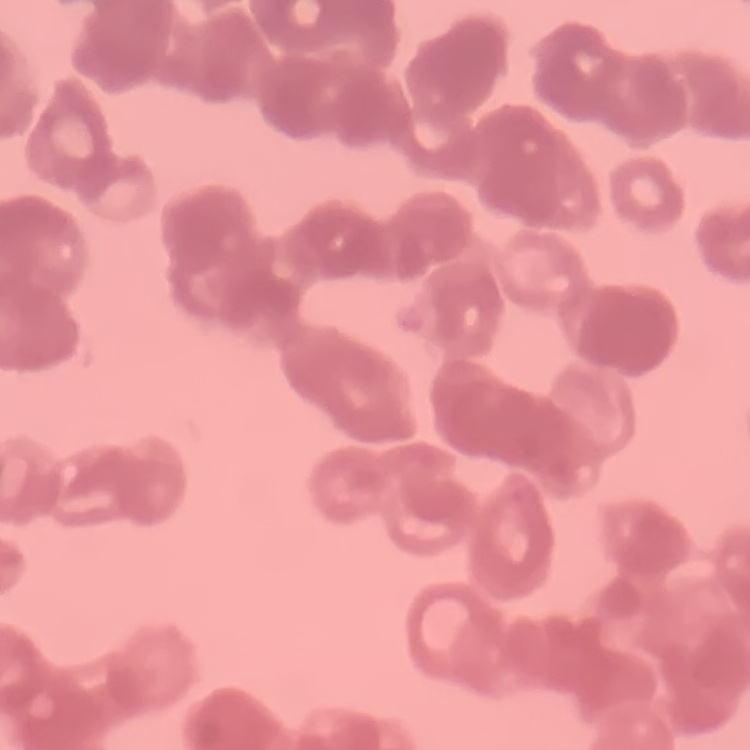

erythrocyte_morphology: rouleaux formation
stain: Field's or Giemsa
image_type: one tile cut from a larger photomicrograph
preparation: thin blood film